Give the position of every leukocyte visible.
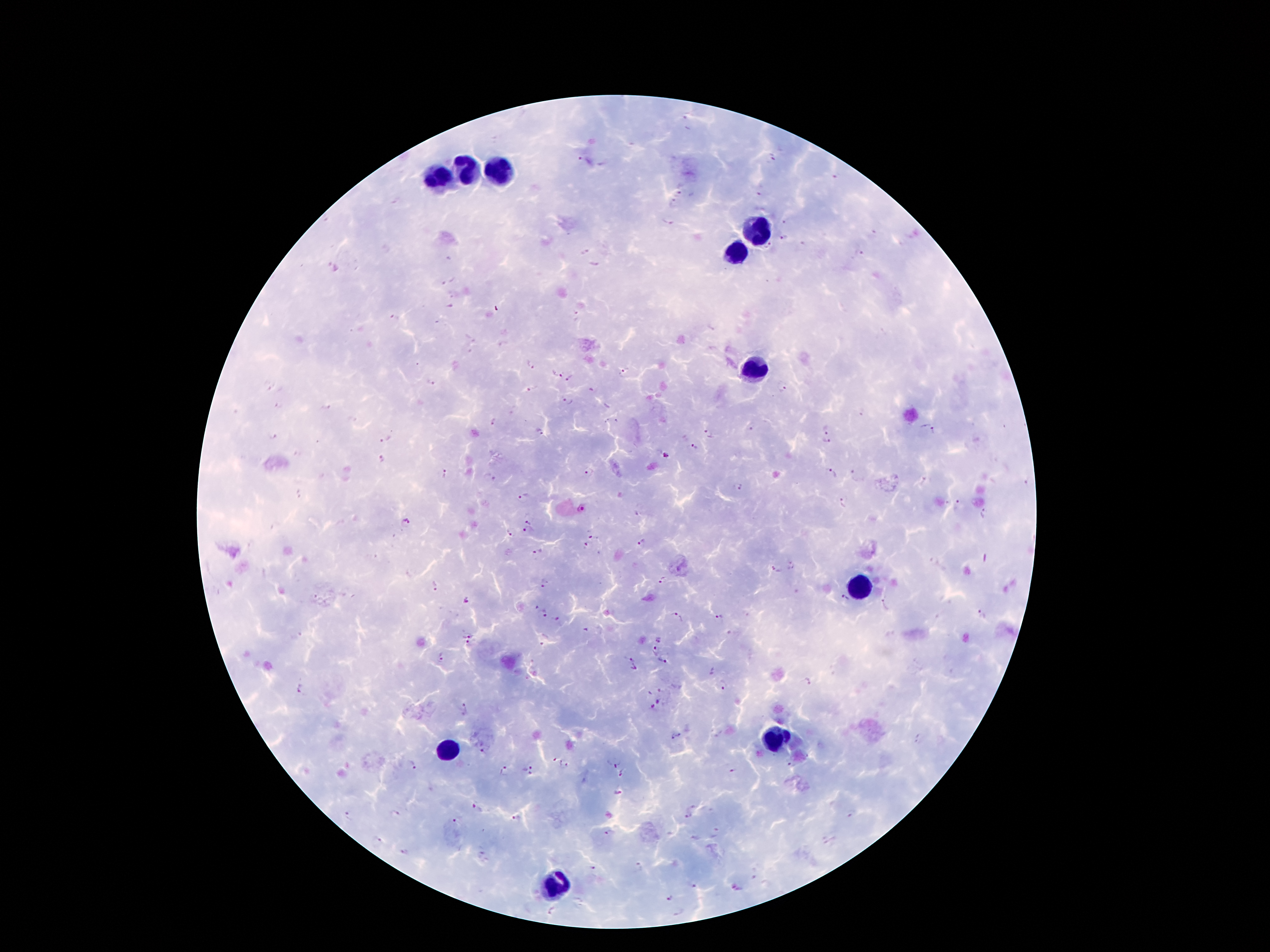

Approximate object centers, in pixels from the top-left corner.
Leukocytes: (x=467, y=166), (x=501, y=169), (x=438, y=177), (x=753, y=232), (x=735, y=253), (x=753, y=371), (x=863, y=589), (x=774, y=739), (x=448, y=749), (x=553, y=880).

Summary:
  - Malaria parasite locations: (x=686, y=117), (x=581, y=158), (x=772, y=159), (x=679, y=193), (x=759, y=193), (x=674, y=204), (x=668, y=223), (x=784, y=223), (x=784, y=238), (x=768, y=248), (x=860, y=254), (x=595, y=263), (x=450, y=281), (x=450, y=306), (x=395, y=319), (x=531, y=365), (x=624, y=372), (x=555, y=374), (x=570, y=379), (x=431, y=383), (x=782, y=385), (x=531, y=389), (x=566, y=400), (x=328, y=406), (x=279, y=407), (x=494, y=422), (x=750, y=429), (x=825, y=430), (x=538, y=432), (x=708, y=432), (x=934, y=432), (x=271, y=436), (x=386, y=439), (x=825, y=442), (x=694, y=447), (x=666, y=455), (x=382, y=459), (x=834, y=472), (x=446, y=474), (x=588, y=474), (x=855, y=476), (x=489, y=478), (x=738, y=486), (x=523, y=498), (x=843, y=502), (x=957, y=502), (x=984, y=513), (x=637, y=514), (x=528, y=520), (x=406, y=522), (x=526, y=531), (x=509, y=532), (x=594, y=536), (x=642, y=544), (x=586, y=545), (x=537, y=553), (x=791, y=565), (x=774, y=572), (x=663, y=581), (x=544, y=583), (x=433, y=586), (x=465, y=599), (x=844, y=599), (x=533, y=605), (x=885, y=605), (x=543, y=614), (x=980, y=614), (x=677, y=617), (x=718, y=617), (x=557, y=619), (x=467, y=633), (x=659, y=640), (x=466, y=644), (x=654, y=651), (x=630, y=655), (x=441, y=659), (x=662, y=662), (x=634, y=669), (x=807, y=682), (x=725, y=687), (x=302, y=691), (x=661, y=700), (x=465, y=709), (x=652, y=709), (x=677, y=736), (x=485, y=749), (x=615, y=761), (x=412, y=766), (x=565, y=766), (x=532, y=769), (x=506, y=770), (x=732, y=770), (x=626, y=773), (x=619, y=793), (x=476, y=808), (x=396, y=815), (x=346, y=816), (x=687, y=817), (x=516, y=818), (x=455, y=824), (x=716, y=832), (x=608, y=833), (x=376, y=843), (x=404, y=853), (x=637, y=866), (x=594, y=868), (x=694, y=883), (x=671, y=899), (x=550, y=911)
  - Patient malaria status: infected with Plasmodium falciparum
  - Field of view: single
  - Magnification: 100x
  - Image size: 1270×952 pixels
  - Capture: smartphone camera through the microscope eyepiece
  - Preparation: thick blood smear
  - Stain: Giemsa